Classify this cell by malaria status.
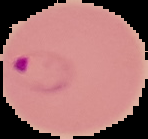
It is parasitized.

From a thin blood smear. The area outside the segmented cell region is set to black. Image is 148×139 pixels.